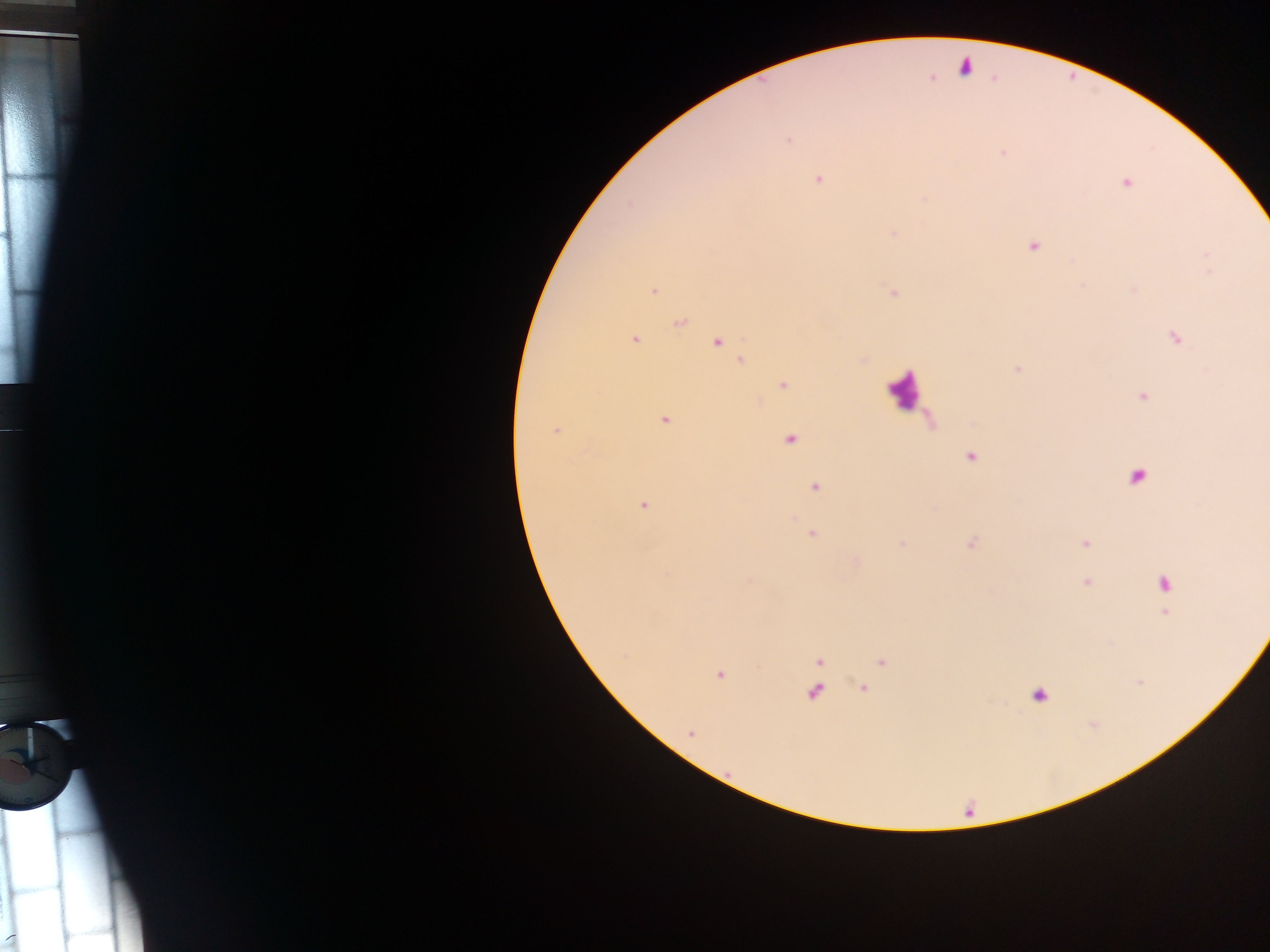

Approximate centers as (x, y) in pixels. Plasmodium parasite locations: (965, 67), (788, 141), (1002, 152), (818, 180), (1126, 183), (893, 233), (1033, 247), (654, 291), (892, 293), (680, 323), (1175, 337), (635, 340), (718, 341), (742, 360), (783, 385), (1144, 397), (665, 420), (556, 430), (790, 439), (971, 457), (1137, 476), (815, 486), (644, 505), (812, 534), (1085, 543), (1087, 583), (1164, 583), (1165, 613), (820, 661), (882, 663), (719, 675), (863, 687), (814, 693), (1039, 695), (691, 732). Leukocyte locations: (903, 389). Image is 1270×952 pixels. Collected in Ghana. Mobile-phone photograph taken through the microscope. Thick blood smear. One field of view.